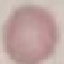 Malaria status: uninfected. Photographed with a smartphone camera at the microscope eyepiece. Giemsa stain. Automatically extracted cell patch, resized to 64 × 64 pixels. Thin blood film.